Draw a bounding box around every leukocyte (white blood cell).
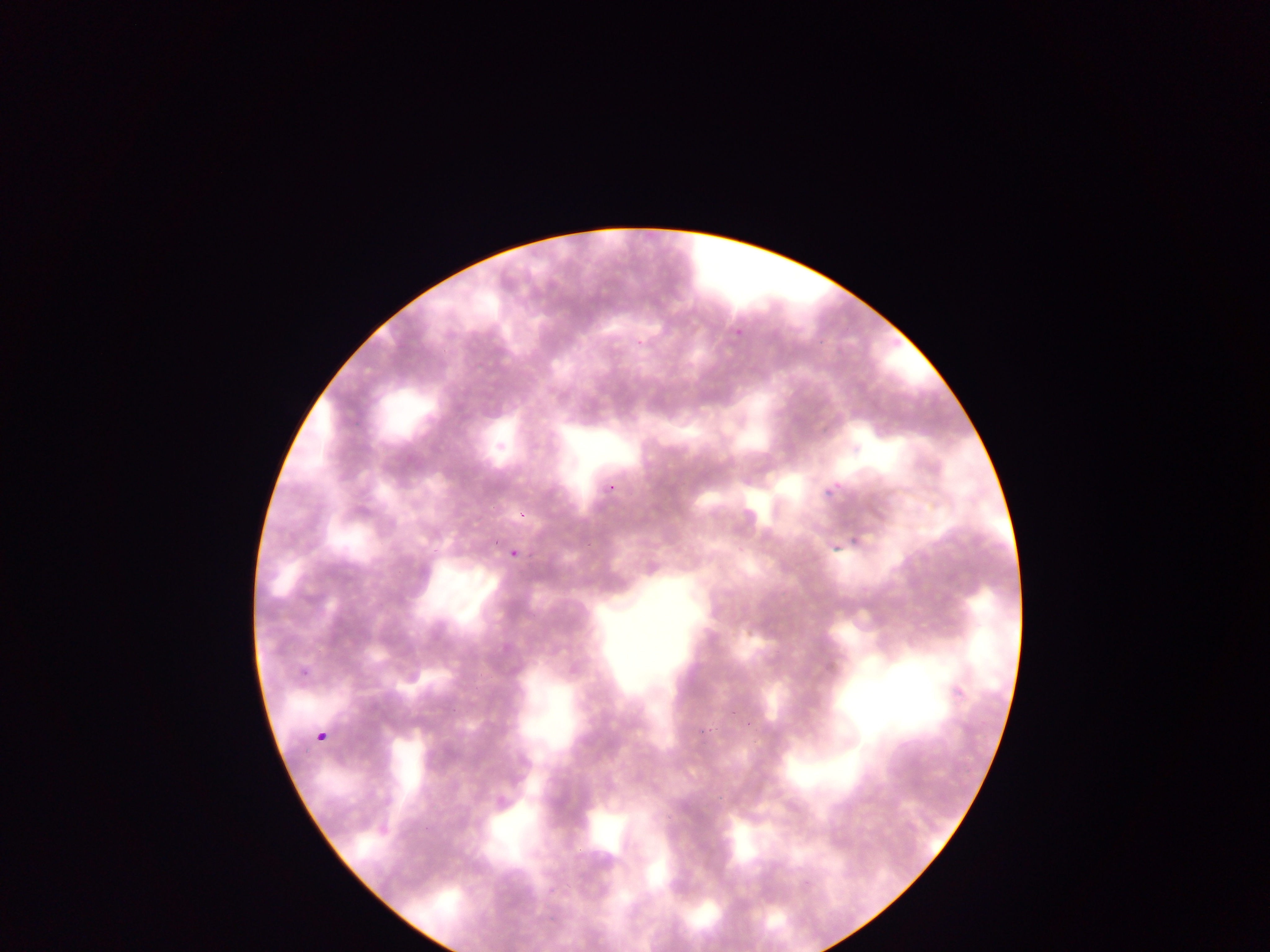

No leukocytes observed.

field of view = single
malaria parasite locations = approximate bounding boxes as (left, top, right, bottom) in pixels: (732, 325, 745, 336), (634, 338, 644, 347), (602, 482, 617, 495), (825, 486, 837, 499), (517, 511, 529, 519), (847, 525, 860, 538), (503, 546, 525, 557), (296, 668, 307, 678), (316, 730, 326, 742)
preparation = thin blood film
capture = mobile-phone photograph through a microscope
image size = 1270×952 pixels
country = Ghana